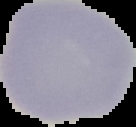
image_type: segmented cell region with the area outside set to black
image_size: 136×127 pixels
preparation: thin blood smear
result: no malaria parasites seen